Classify this cell by malaria status.
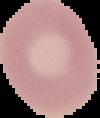

It is uninfected.

Image is 100×118 pixels. The area outside the segmented cell region is set to black. From a thin blood smear.